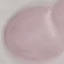
Summary:
  - Result: negative for malaria parasites
  - Image type: automatically extracted cell patch, resized to 64 × 64 pixels
  - Capture: smartphone through the microscope eyepiece
  - Preparation: thin blood smear
  - Stain: Giemsa